Name the parasite shown.
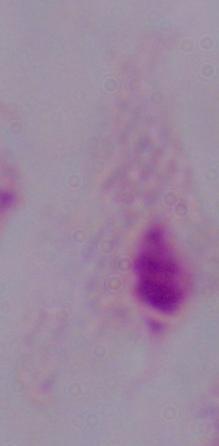
This is a trichomonad.

Summary:
  - Modality: photomicrograph
  - Magnification: 1000x